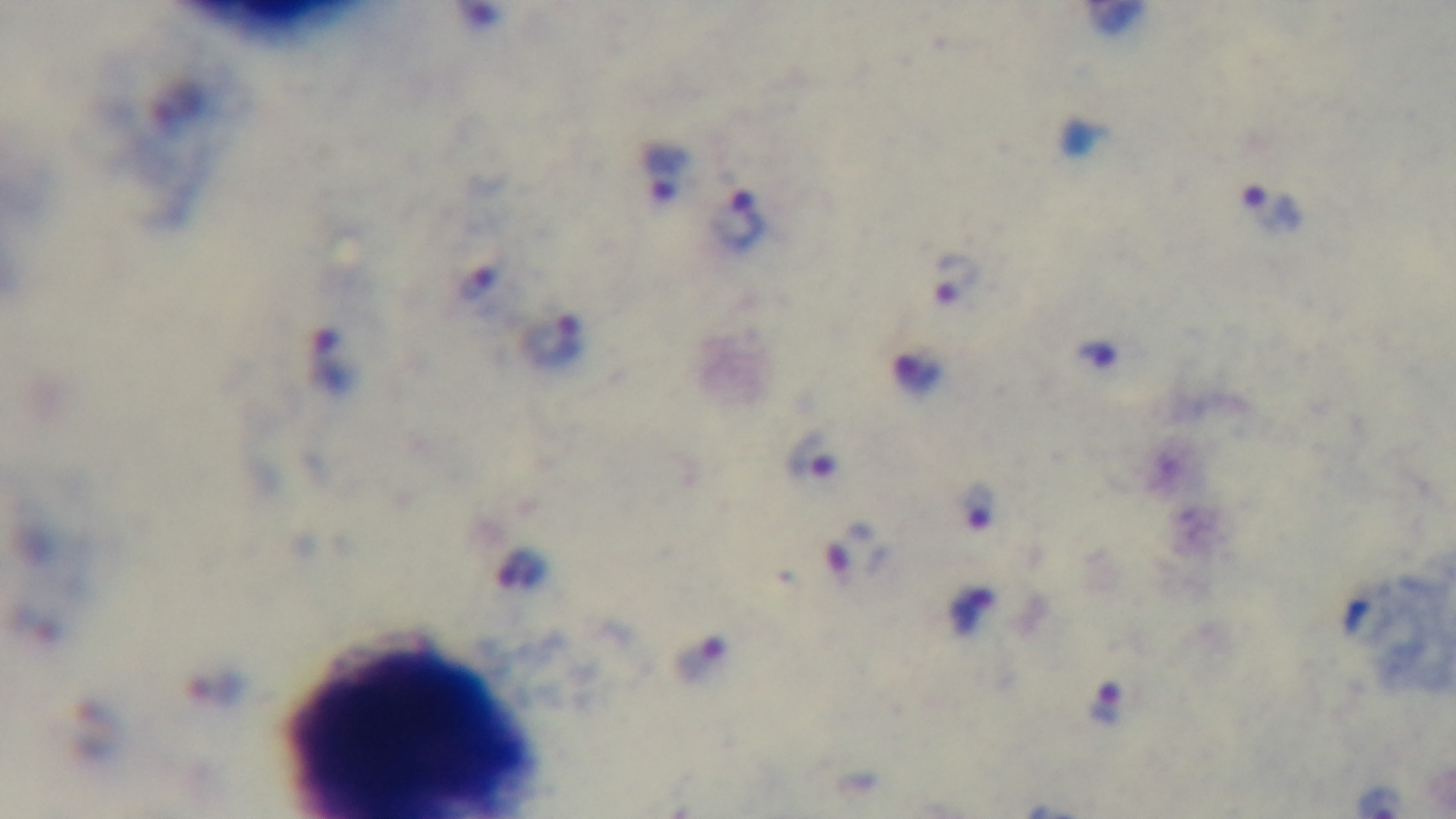
Summary:
  - Preparation: thick smear
  - Malaria status: positive
  - Capture: mounted 4K digital camera
  - Objective: 100x oil immersion
  - Field of view: single
  - Stain: Giemsa
  - Modality: light microscopy